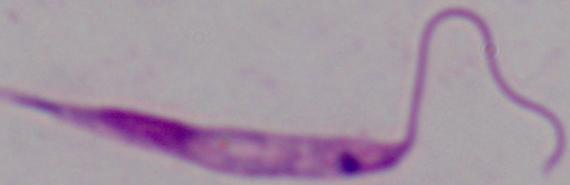

identification: Leishmania
modality: micrograph
magnification: 1000x